Give the preparation type.
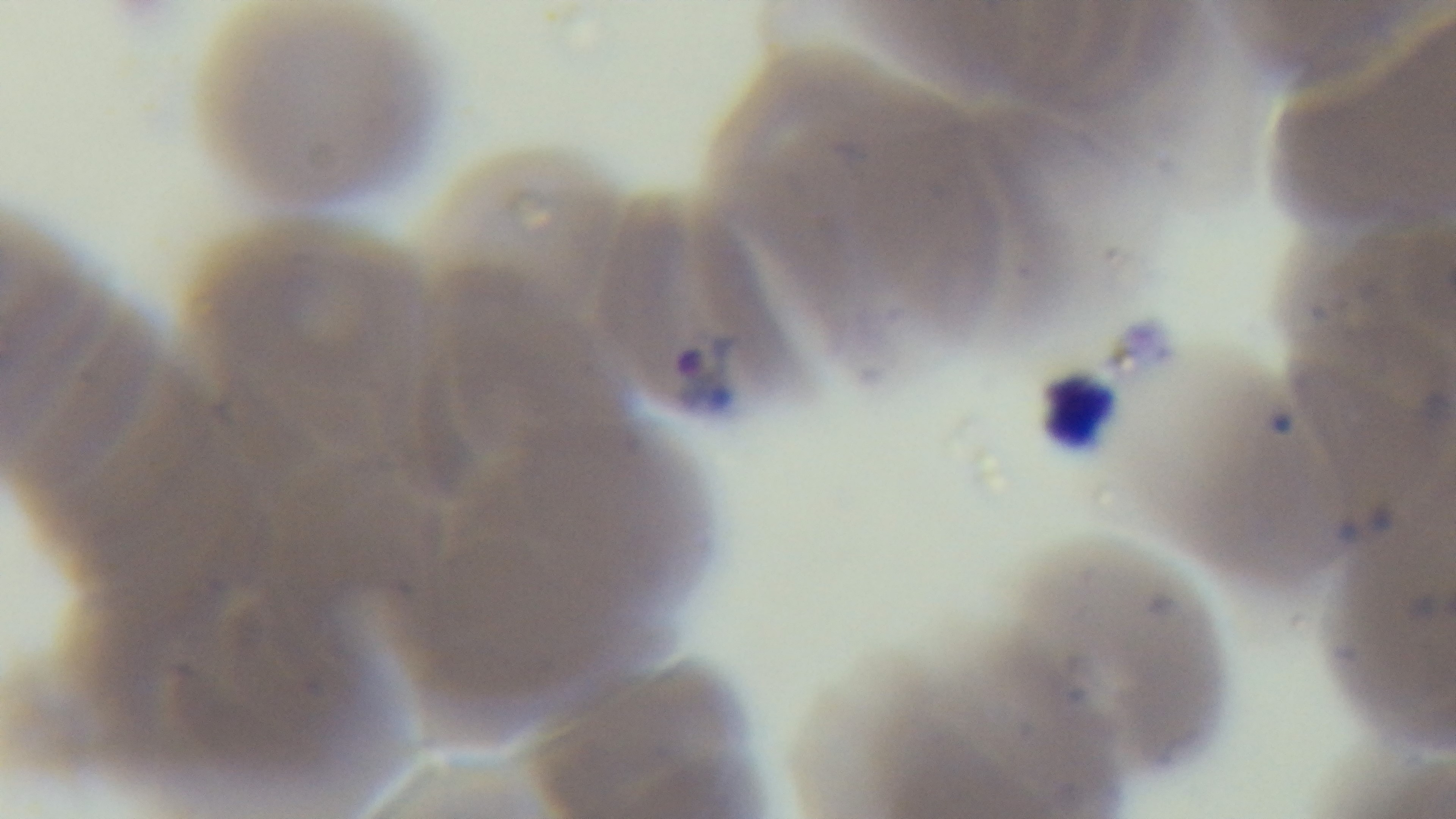
A thin smear.

Summary:
  - Field of view: single
  - Malaria status: positive
  - Capture: mounted 4K digital camera
  - Stain: Giemsa
  - Objective: 100x oil immersion
  - Modality: light microscopy